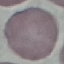

Summary:
  - Result: negative for malaria parasites
  - Capture: smartphone through the microscope eyepiece
  - Preparation: thin smear
  - Image type: automatically extracted cell patch, resized to 64 × 64 pixels
  - Stain: Giemsa